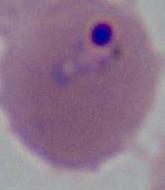

{
  "identification": "Plasmodium",
  "magnification": "400x or 1000x",
  "modality": "photomicrograph"
}